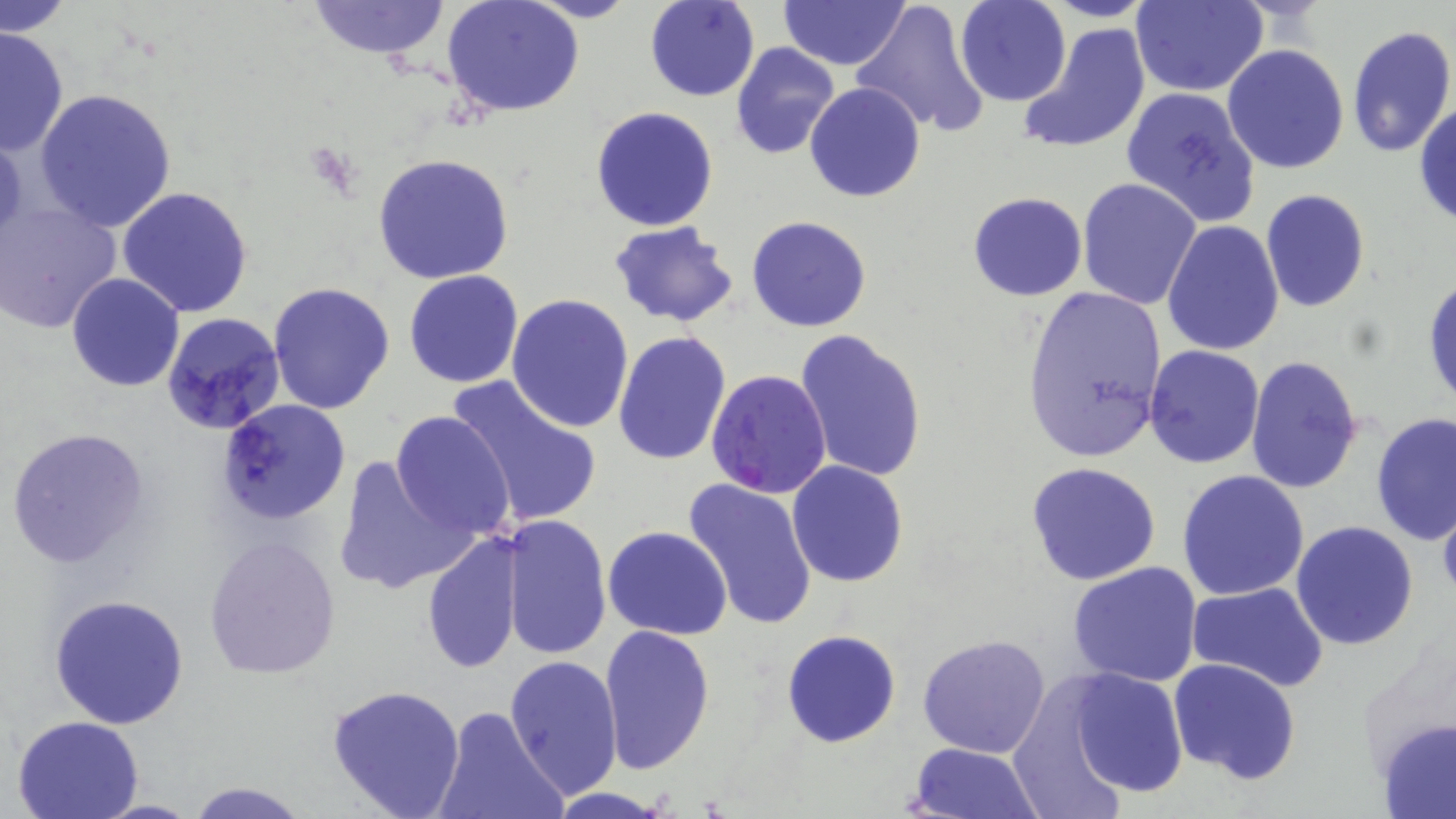
Summary:
  - Coordinate format: approximate bounding boxes as [x1, y1, x2, y2] in pixels
  - Plasmodium falciparum-infected red blood cell locations: [706, 369, 832, 501]
  - Uninfected red blood cell locations: [3, 0, 72, 38], [307, 0, 452, 60], [443, 0, 584, 119], [645, 0, 760, 102], [778, 0, 909, 70], [848, 0, 993, 140], [954, 0, 1072, 106], [1129, 1, 1268, 96], [1019, 22, 1150, 156], [1343, 24, 1456, 162], [0, 26, 68, 158], [731, 42, 840, 160], [1222, 44, 1350, 175], [805, 82, 926, 202], [1120, 86, 1261, 226], [34, 89, 177, 233], [1415, 100, 1456, 229], [589, 106, 719, 231], [0, 130, 27, 247], [371, 153, 516, 286], [1077, 178, 1202, 309], [118, 187, 255, 319], [1259, 189, 1369, 312], [968, 191, 1087, 300], [0, 199, 122, 333], [746, 214, 873, 332], [609, 220, 738, 327], [1162, 220, 1285, 358], [403, 269, 523, 387], [1423, 271, 1456, 414], [66, 274, 184, 392], [268, 281, 396, 415], [1020, 286, 1168, 462], [507, 293, 635, 433], [160, 311, 287, 436], [794, 328, 928, 483], [612, 331, 732, 468], [1143, 344, 1265, 469], [1244, 356, 1364, 494], [441, 374, 602, 531], [214, 399, 351, 525], [390, 410, 514, 540], [1371, 412, 1455, 544], [3, 426, 152, 571], [333, 452, 474, 596], [786, 461, 910, 588], [1025, 461, 1165, 587], [1177, 470, 1309, 599], [683, 476, 819, 631], [1437, 488, 1456, 607], [501, 513, 611, 660], [1290, 520, 1419, 650], [603, 527, 731, 640], [421, 529, 526, 675], [204, 535, 340, 679], [1067, 561, 1203, 686], [1186, 582, 1328, 693], [49, 592, 191, 728], [597, 623, 717, 775], [781, 629, 901, 748], [918, 633, 1052, 758], [503, 654, 622, 802], [1168, 658, 1302, 785], [1052, 664, 1195, 802], [325, 682, 467, 819], [434, 707, 568, 819], [12, 715, 146, 819], [1377, 717, 1456, 818], [906, 742, 1044, 819], [183, 779, 312, 818], [544, 788, 676, 818], [90, 798, 201, 818]
  - Slide-level diagnosis: Plasmodium falciparum
  - Stain: May-Grünwald-Giemsa
  - Field of view: one of a larger specimen
  - Preparation: thin blood film
  - Magnification: 1000x
  - Modality: light microscopy
  - Image size: 1456×819 pixels